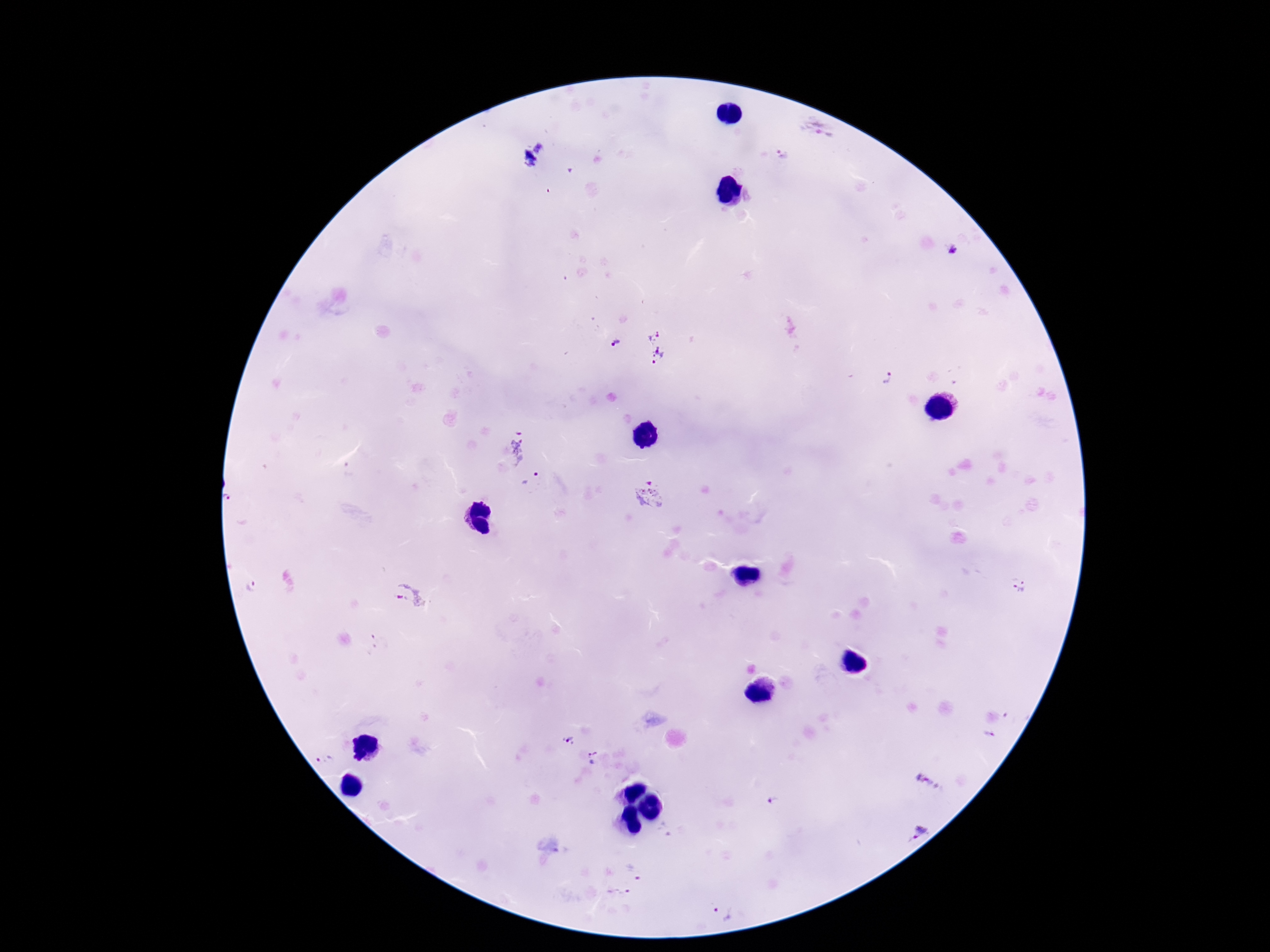
Approximate centers as (x, y) in pixels.
Summary:
  - Plasmodium parasite locations: (817, 130), (541, 145), (781, 155), (527, 162), (955, 250), (652, 335), (617, 342), (658, 355), (888, 377), (518, 447), (530, 479), (652, 496), (1019, 586), (255, 587), (408, 596), (990, 736), (568, 742), (592, 758), (324, 759), (929, 785), (918, 831), (638, 870), (617, 894), (722, 913)
  - Patient malaria status: infected
  - Image size: 1270×952 pixels
  - Field of view: single
  - Magnification: 100x
  - Stain: Giemsa
  - Preparation: thick blood smear
  - Capture: smartphone camera through the microscope eyepiece